Give the extent of all Plasmodium ovale-infected red blood cells.
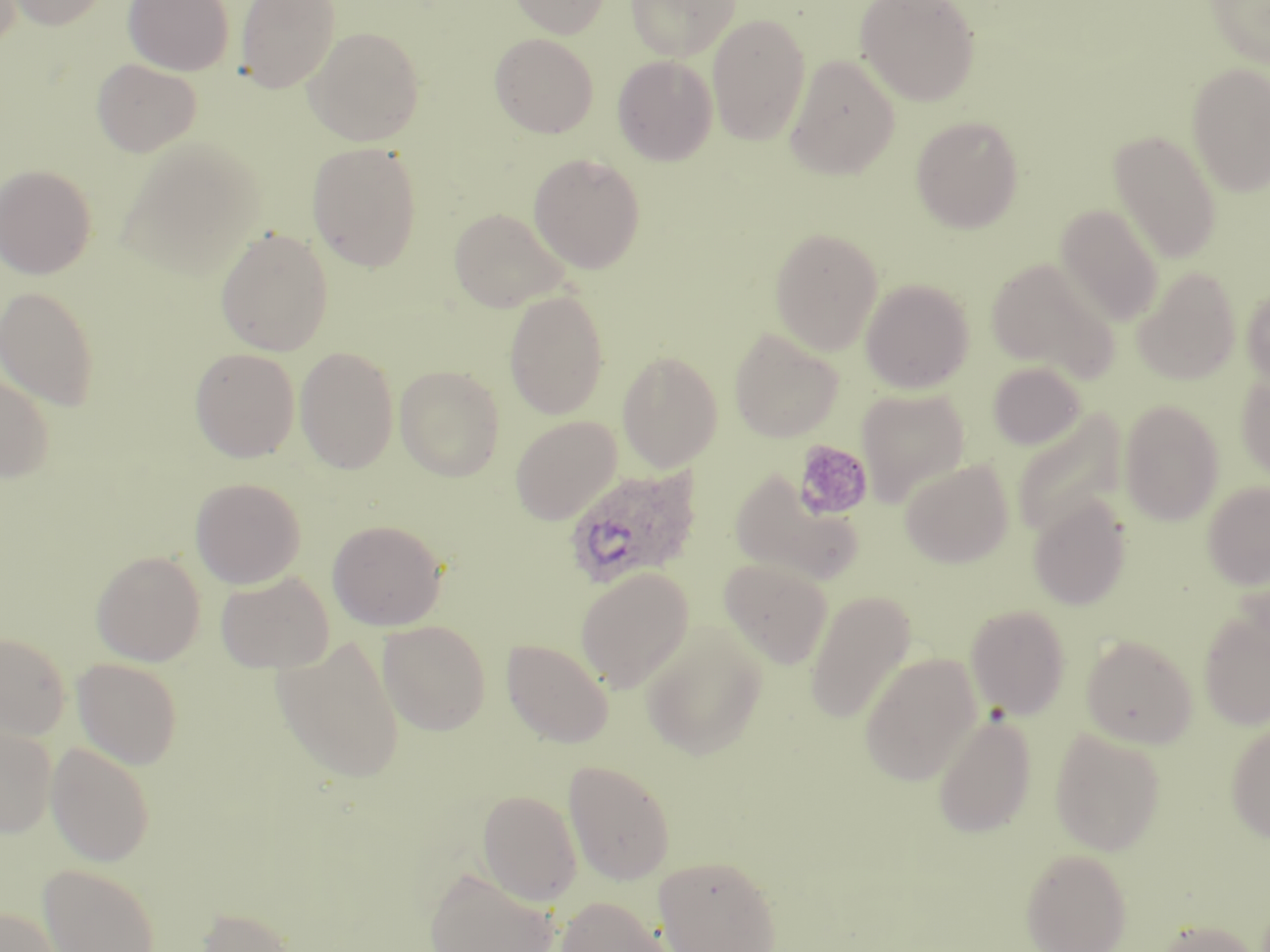
Approximate bounding boxes as (x1,y1)-(x2,y2) corner pairs in pixels.
Plasmodium ovale-infected red blood cells: (563,465)-(703,589).

Summary:
  - Uninfected red blood cell locations: (4,0)-(110,30), (123,0)-(234,76), (235,0)-(339,93), (509,0)-(610,38), (626,0)-(741,61), (855,0)-(981,106), (1206,0)-(1270,68), (707,14)-(810,146), (305,26)-(425,146), (490,33)-(598,138), (612,55)-(718,165), (785,55)-(900,179), (91,58)-(202,157), (1187,63)-(1270,197), (911,116)-(1024,233), (1110,130)-(1222,263), (118,137)-(264,279), (307,142)-(423,271), (528,153)-(646,273), (0,164)-(96,279), (1055,204)-(1164,326), (448,207)-(568,312), (215,227)-(333,356), (769,227)-(884,354), (986,256)-(1120,382), (1133,267)-(1241,384), (861,279)-(974,394), (1241,284)-(1270,390), (0,285)-(100,410), (503,289)-(610,420), (729,328)-(843,443), (294,346)-(399,474), (190,347)-(300,462), (617,350)-(723,471), (987,362)-(1087,450), (395,365)-(505,481), (1236,373)-(1270,482), (0,374)-(54,483), (857,389)-(970,507), (1119,399)-(1224,526), (1012,409)-(1126,540), (510,415)-(621,524), (900,460)-(1013,568), (729,471)-(862,586), (190,477)-(306,588), (1202,481)-(1270,589), (1028,495)-(1133,610), (327,519)-(447,631), (90,550)-(206,666), (719,558)-(832,669), (575,567)-(694,693), (215,572)-(334,674), (805,590)-(915,724), (965,604)-(1071,719), (1198,608)-(1270,729), (378,620)-(491,735), (641,623)-(767,760), (0,633)-(69,740), (1081,634)-(1197,748), (272,636)-(405,783), (501,639)-(613,748), (860,653)-(982,787), (72,658)-(182,769), (931,711)-(1037,838), (1226,719)-(1270,843), (0,723)-(57,838), (1049,729)-(1166,855), (46,743)-(155,866), (563,759)-(676,885), (477,790)-(582,905), (1020,848)-(1133,952), (653,854)-(783,952), (38,863)-(161,952), (423,865)-(559,952), (554,896)-(675,952), (196,906)-(299,952), (0,907)-(61,952), (1151,919)-(1262,952)
  - Platelet locations: (792,440)-(874,521)
  - Slide-level diagnosis: Plasmodium ovale
  - Magnification: 1000x
  - Preparation: thin blood film
  - Stain: May-Grünwald-Giemsa
  - Image size: 1270×952 pixels
  - Modality: light microscopy
  - Field of view: one of a larger specimen